Give the extent of all Plasmodium ovale-infected red blood cells.
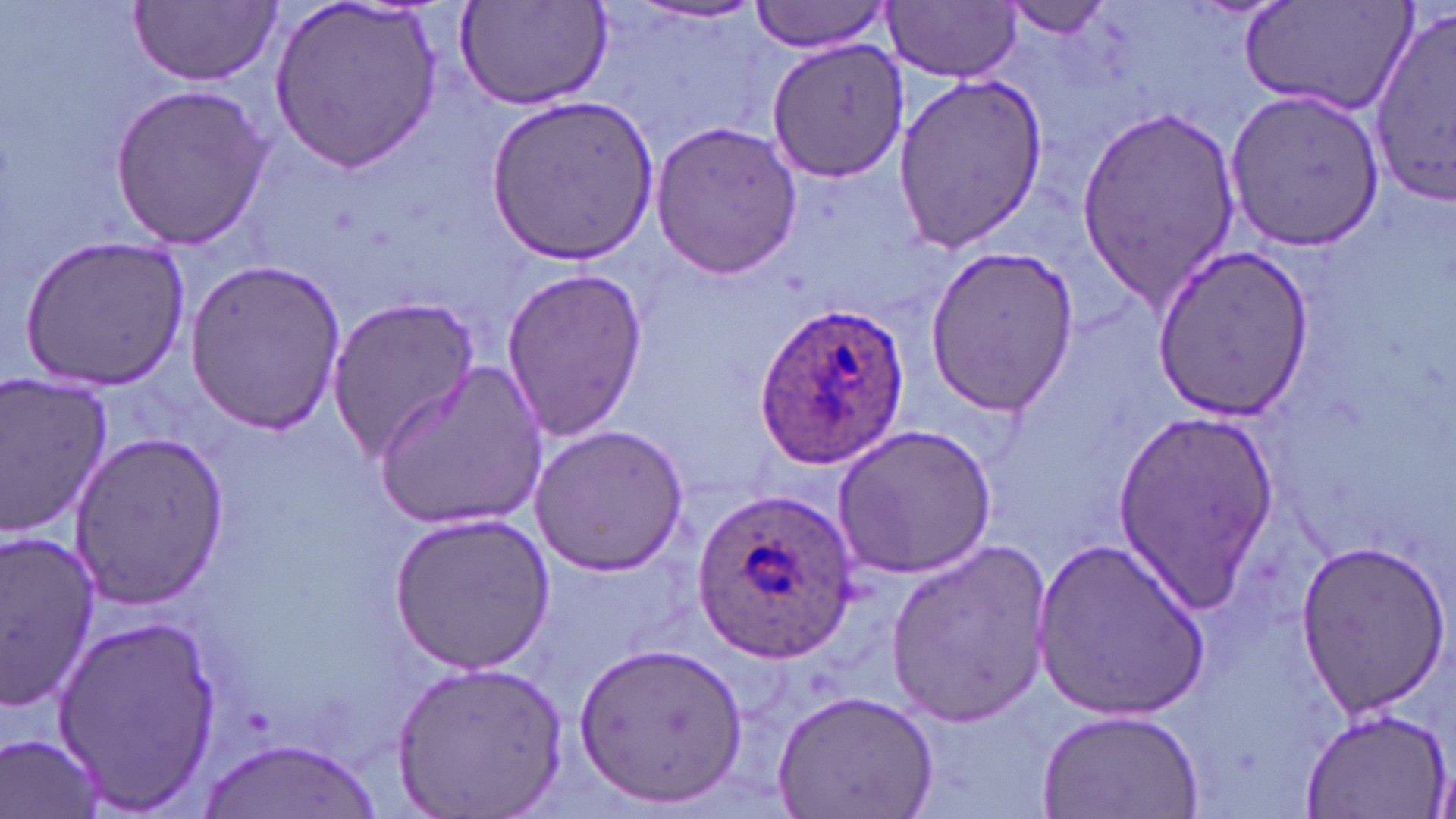
Approximate bounding boxes as named x1/y1/x2/y2 corners in pixels.
Plasmodium ovale-infected red blood cells: (x1=751, y1=303, x2=909, y2=470), (x1=694, y1=486, x2=860, y2=663).

Uninfected red blood cell locations: (x1=268, y1=0, x2=445, y2=171), (x1=749, y1=0, x2=893, y2=53), (x1=999, y1=0, x2=1121, y2=42), (x1=129, y1=1, x2=282, y2=87), (x1=1239, y1=1, x2=1418, y2=117), (x1=632, y1=2, x2=765, y2=26), (x1=884, y1=2, x2=1021, y2=82), (x1=453, y1=3, x2=614, y2=113), (x1=1368, y1=8, x2=1456, y2=207), (x1=766, y1=36, x2=912, y2=184), (x1=892, y1=72, x2=1050, y2=255), (x1=109, y1=82, x2=272, y2=250), (x1=1223, y1=86, x2=1386, y2=253), (x1=483, y1=93, x2=661, y2=266), (x1=1077, y1=105, x2=1244, y2=306), (x1=648, y1=118, x2=803, y2=280), (x1=18, y1=232, x2=191, y2=391), (x1=922, y1=245, x2=1078, y2=416), (x1=1149, y1=246, x2=1319, y2=418), (x1=182, y1=260, x2=350, y2=430), (x1=500, y1=267, x2=648, y2=441), (x1=326, y1=291, x2=482, y2=462), (x1=374, y1=363, x2=549, y2=533), (x1=0, y1=372, x2=115, y2=540), (x1=1109, y1=408, x2=1279, y2=605), (x1=833, y1=422, x2=997, y2=579), (x1=526, y1=423, x2=690, y2=577), (x1=68, y1=428, x2=229, y2=608), (x1=386, y1=510, x2=556, y2=674), (x1=0, y1=532, x2=103, y2=706), (x1=1031, y1=537, x2=1211, y2=720), (x1=1293, y1=537, x2=1449, y2=716), (x1=886, y1=540, x2=1056, y2=723), (x1=55, y1=615, x2=224, y2=808), (x1=575, y1=639, x2=749, y2=808), (x1=393, y1=659, x2=569, y2=816), (x1=772, y1=688, x2=941, y2=819), (x1=1301, y1=703, x2=1452, y2=819), (x1=1036, y1=712, x2=1202, y2=819), (x1=1, y1=732, x2=106, y2=819), (x1=200, y1=739, x2=383, y2=818). Slide-level diagnosis: Plasmodium ovale. Thin blood film. One field of a larger specimen. May-Grünwald-Giemsa stain. Image is 1456×819 pixels. Captured at 1000x magnification. Optical microscopy.